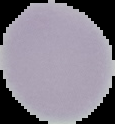

Summary:
  - Image type: segmented cell region with the area outside set to black
  - Preparation: thin blood film
  - Image size: 115×124 pixels
  - Malaria status: uninfected